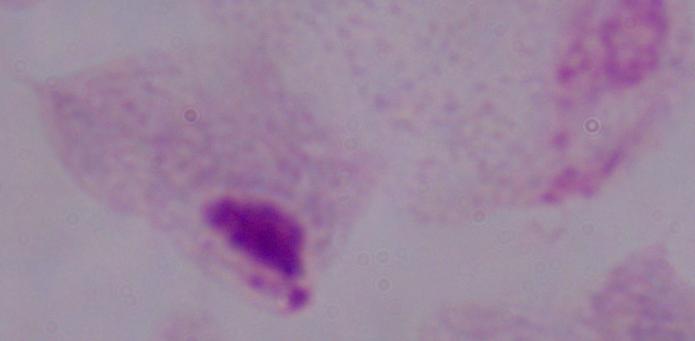

Summary:
  - Modality: photomicrograph
  - Magnification: 1000x
  - Identification: trichomonad